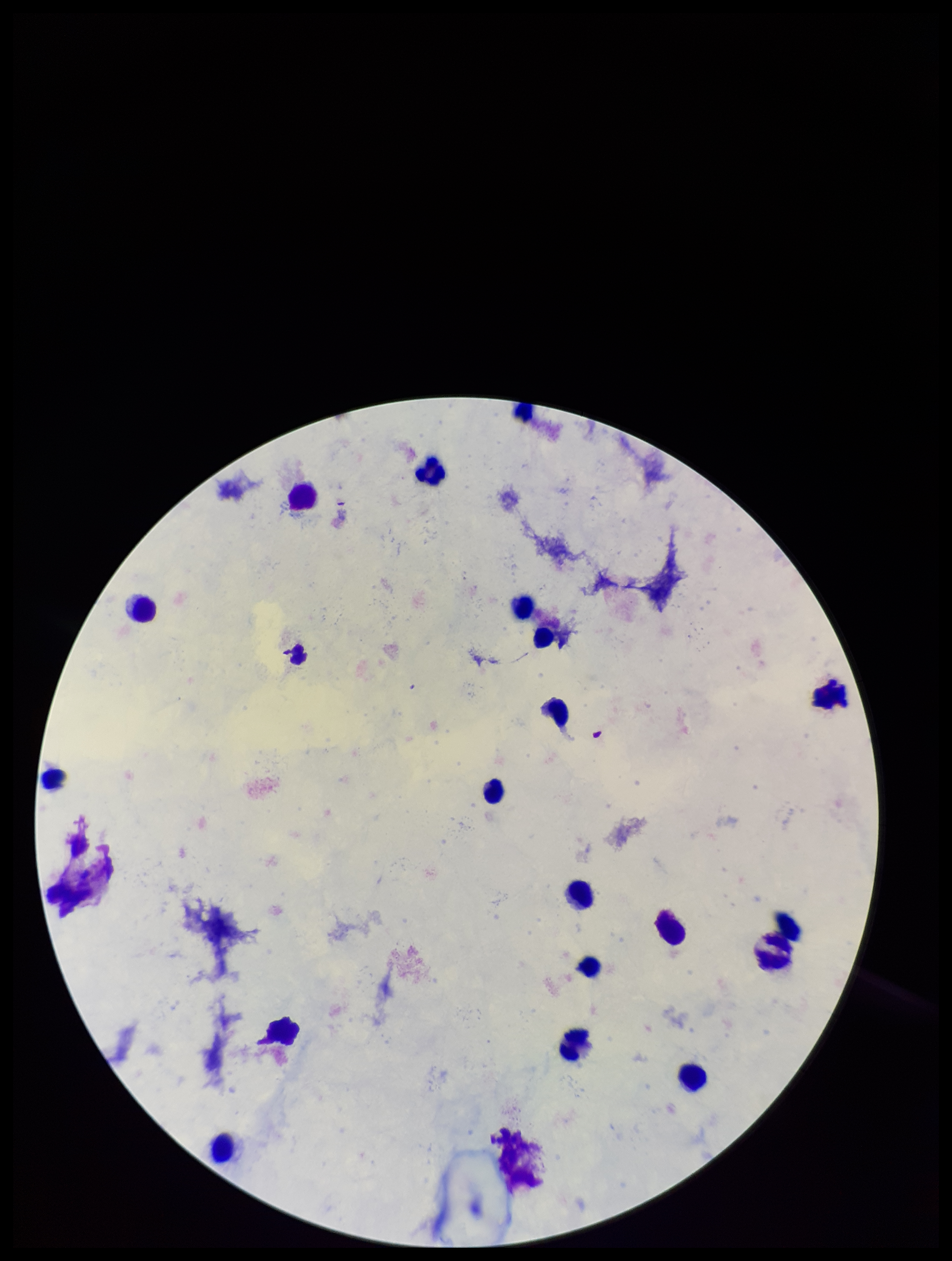

capture = smartphone photograph through the microscope eyepiece
patient malaria status = negative
Plasmodium parasites = none detected
stain = Giemsa
leukocyte count = 18
preparation = thick
field of view = single
image size = 952×1261 pixels
parasite count = 0